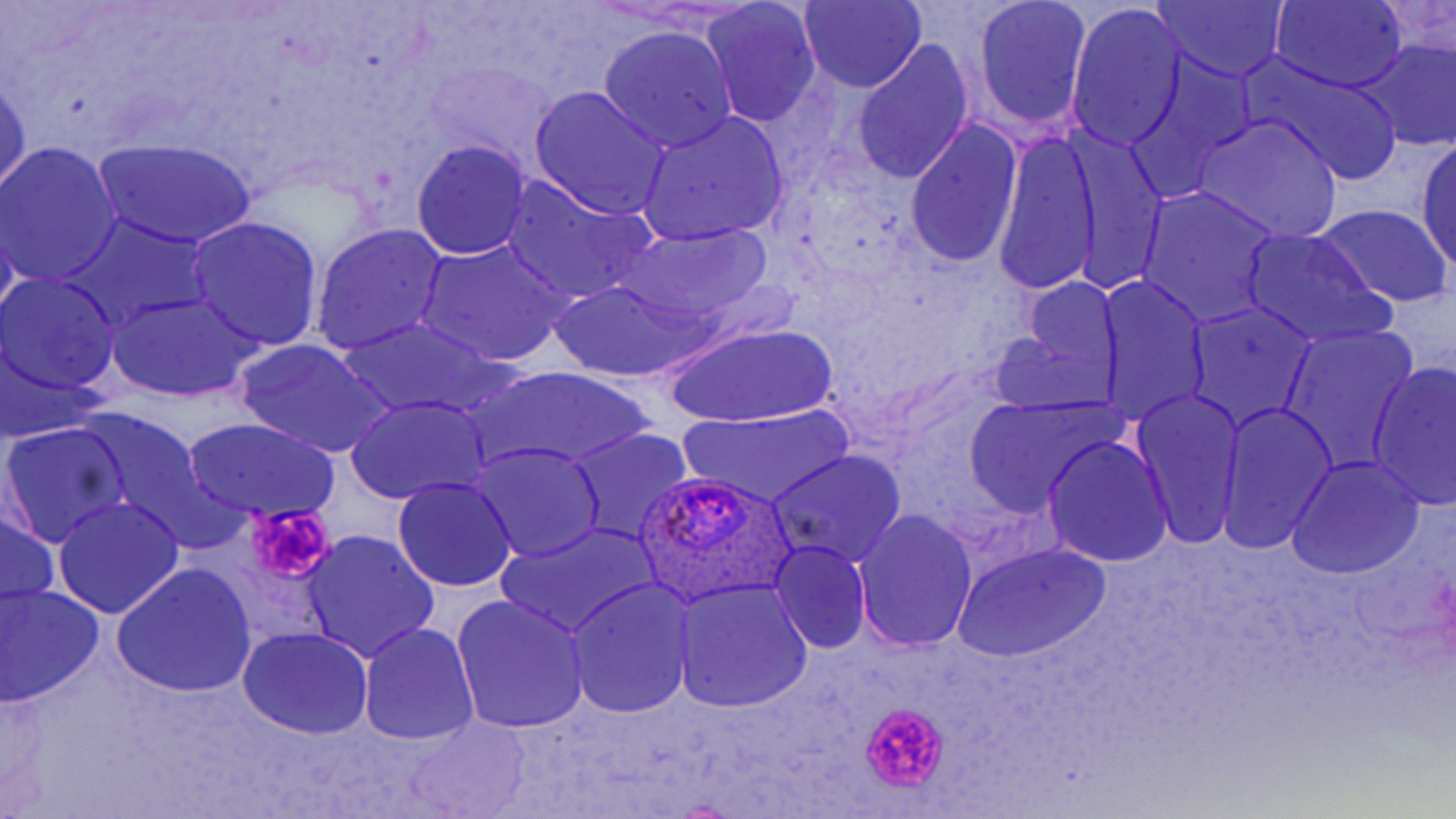

Approximate bounding boxes as named x1/y1/x2/y2 corners in pixels. Uninfected red blood cell locations: (x1=971, y1=0, x2=1092, y2=133), (x1=1269, y1=0, x2=1409, y2=93), (x1=1153, y1=1, x2=1289, y2=82), (x1=700, y1=2, x2=823, y2=125), (x1=799, y1=2, x2=927, y2=91), (x1=1069, y1=7, x2=1186, y2=146), (x1=598, y1=26, x2=739, y2=153), (x1=1355, y1=34, x2=1456, y2=153), (x1=851, y1=39, x2=975, y2=186), (x1=1256, y1=66, x2=1405, y2=186), (x1=0, y1=73, x2=30, y2=198), (x1=528, y1=86, x2=672, y2=219), (x1=636, y1=112, x2=790, y2=246), (x1=1193, y1=114, x2=1343, y2=240), (x1=906, y1=119, x2=1023, y2=269), (x1=995, y1=132, x2=1103, y2=298), (x1=94, y1=139, x2=259, y2=249), (x1=411, y1=140, x2=531, y2=258), (x1=1071, y1=140, x2=1168, y2=289), (x1=1415, y1=140, x2=1456, y2=268), (x1=1, y1=144, x2=121, y2=285), (x1=502, y1=177, x2=652, y2=302), (x1=1137, y1=187, x2=1280, y2=325), (x1=1313, y1=204, x2=1454, y2=307), (x1=187, y1=217, x2=324, y2=352), (x1=72, y1=221, x2=202, y2=328), (x1=616, y1=221, x2=774, y2=328), (x1=310, y1=223, x2=448, y2=356), (x1=1241, y1=229, x2=1391, y2=349), (x1=417, y1=240, x2=569, y2=366), (x1=1, y1=274, x2=122, y2=396), (x1=1098, y1=274, x2=1210, y2=425), (x1=552, y1=279, x2=688, y2=382), (x1=1011, y1=281, x2=1125, y2=401), (x1=111, y1=290, x2=259, y2=400), (x1=1183, y1=301, x2=1318, y2=430), (x1=339, y1=318, x2=501, y2=418), (x1=667, y1=324, x2=837, y2=427), (x1=1280, y1=324, x2=1419, y2=472), (x1=990, y1=330, x2=1111, y2=416), (x1=235, y1=340, x2=393, y2=459), (x1=1367, y1=362, x2=1455, y2=509), (x1=477, y1=367, x2=652, y2=472), (x1=1132, y1=387, x2=1245, y2=551), (x1=346, y1=395, x2=489, y2=504), (x1=963, y1=397, x2=1119, y2=516), (x1=1216, y1=400, x2=1337, y2=555), (x1=680, y1=406, x2=853, y2=508), (x1=86, y1=415, x2=210, y2=535), (x1=185, y1=417, x2=337, y2=523), (x1=3, y1=425, x2=129, y2=545), (x1=565, y1=429, x2=694, y2=545), (x1=1043, y1=436, x2=1174, y2=566), (x1=472, y1=444, x2=605, y2=563), (x1=769, y1=449, x2=906, y2=570), (x1=1286, y1=457, x2=1426, y2=578), (x1=394, y1=475, x2=518, y2=593), (x1=52, y1=496, x2=183, y2=619), (x1=0, y1=509, x2=58, y2=612), (x1=854, y1=510, x2=978, y2=655), (x1=499, y1=521, x2=658, y2=641), (x1=299, y1=531, x2=439, y2=664), (x1=769, y1=541, x2=871, y2=654), (x1=954, y1=542, x2=1112, y2=664), (x1=114, y1=564, x2=256, y2=696), (x1=566, y1=580, x2=695, y2=718), (x1=671, y1=581, x2=812, y2=712), (x1=0, y1=584, x2=102, y2=708), (x1=450, y1=596, x2=590, y2=734), (x1=360, y1=622, x2=480, y2=746), (x1=237, y1=626, x2=374, y2=741), (x1=408, y1=715, x2=527, y2=819). Platelet locations: (x1=244, y1=500, x2=341, y2=579), (x1=859, y1=701, x2=949, y2=791). Plasmodium ovale-infected red blood cell locations: (x1=628, y1=470, x2=799, y2=610). Slide-level diagnosis: Plasmodium ovale. Light microscopy. May-Grünwald-Giemsa stain. Captured at 1000x magnification. Thin blood film. Image is 1456×819 pixels. One field of a larger specimen.